Report the malaria status of this cell.
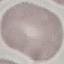
It is uninfected.

Summary:
  - Stain: Giemsa
  - Image type: cell patch, automatically extracted from a larger field of view and resized to 64 × 64 pixels
  - Preparation: thin smear
  - Capture: smartphone through the microscope eyepiece